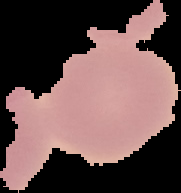

malaria status = uninfected
preparation = thin blood smear
image type = segmented cell region with the area outside set to black
image size = 181×193 pixels